State which parasite is depicted.
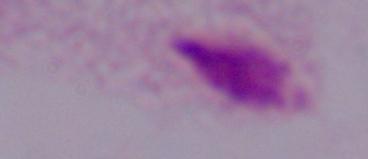

A trichomonad.

Summary:
  - Modality: photomicrograph
  - Magnification: 1000x